State which parasite is depicted.
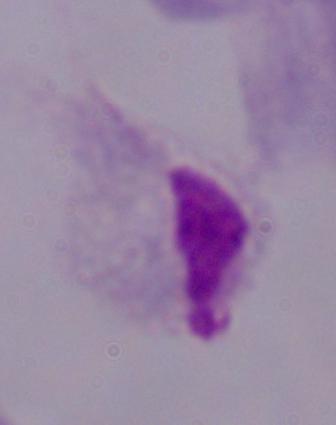
This is a trichomonad.

Summary:
  - Magnification: 1000x
  - Modality: micrograph